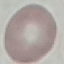
Malaria status: uninfected. Giemsa-stained preparation. Photographed with a smartphone camera at the microscope eyepiece. Cell patch, automatically extracted from a larger field of view and resized to 64 × 64 pixels. Thin blood smear.